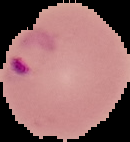
Summary:
  - Image size: 130×142 pixels
  - Preparation: thin blood film
  - Image type: segmented cell region on a black background
  - Malaria status: parasitized